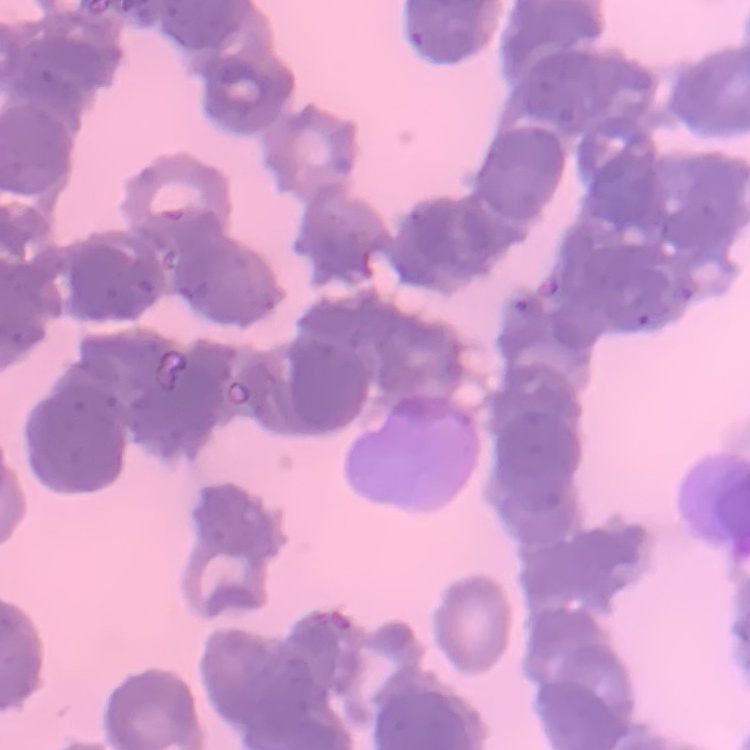
red blood cell morphology = rouleaux formation
stain = Field's or Giemsa
image type = one tile cut from a larger photomicrograph
preparation = thin blood film